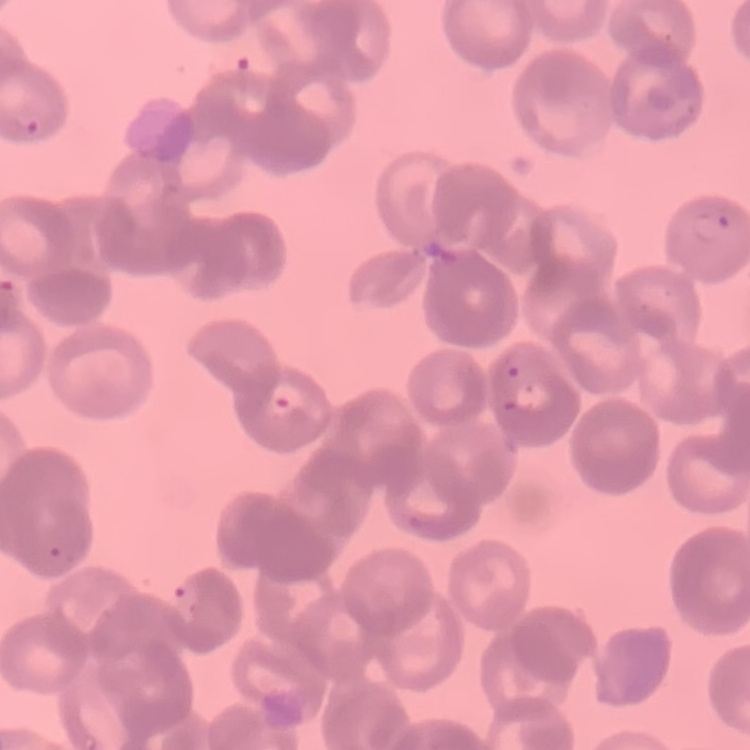

red blood cell morphology = rouleaux formation
image type = one tile cut from a larger photomicrograph
preparation = thin peripheral smear
stain = Field's or Giemsa